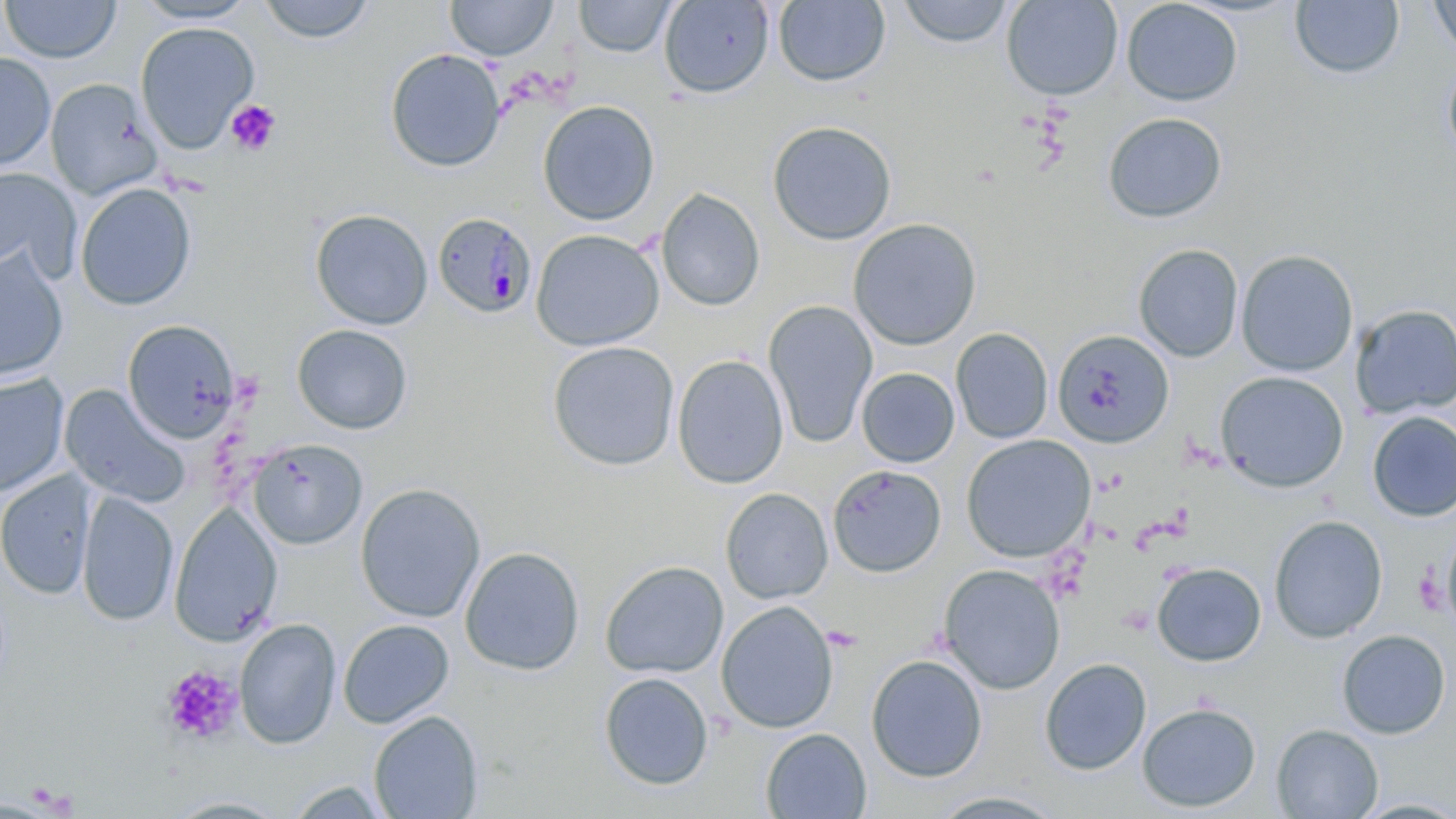 Approximate bounding boxes as named x1/y1/x2/y2 corners in pixels. Platelet locations: (x1=225, y1=100, x2=281, y2=156), (x1=1413, y1=563, x2=1446, y2=620), (x1=161, y1=665, x2=242, y2=744). Uninfected red blood cell locations: (x1=131, y1=0, x2=260, y2=24), (x1=256, y1=0, x2=377, y2=44), (x1=1000, y1=0, x2=1123, y2=101), (x1=1121, y1=0, x2=1243, y2=106), (x1=1427, y1=0, x2=1456, y2=58), (x1=1, y1=1, x2=122, y2=63), (x1=445, y1=1, x2=558, y2=61), (x1=574, y1=1, x2=676, y2=58), (x1=658, y1=1, x2=774, y2=99), (x1=772, y1=1, x2=891, y2=87), (x1=897, y1=1, x2=1014, y2=48), (x1=1290, y1=1, x2=1404, y2=80), (x1=135, y1=21, x2=259, y2=154), (x1=385, y1=48, x2=506, y2=173), (x1=0, y1=51, x2=56, y2=172), (x1=1442, y1=55, x2=1456, y2=164), (x1=45, y1=79, x2=161, y2=199), (x1=537, y1=100, x2=660, y2=226), (x1=1103, y1=112, x2=1227, y2=224), (x1=767, y1=120, x2=897, y2=245), (x1=0, y1=167, x2=82, y2=282), (x1=75, y1=182, x2=197, y2=311), (x1=656, y1=188, x2=765, y2=311), (x1=310, y1=208, x2=433, y2=329), (x1=847, y1=218, x2=982, y2=350), (x1=530, y1=229, x2=665, y2=351), (x1=1134, y1=243, x2=1244, y2=362), (x1=0, y1=249, x2=69, y2=384), (x1=1236, y1=249, x2=1359, y2=377), (x1=763, y1=300, x2=878, y2=448), (x1=1349, y1=305, x2=1456, y2=419), (x1=122, y1=320, x2=242, y2=443), (x1=292, y1=324, x2=413, y2=434), (x1=950, y1=327, x2=1054, y2=444), (x1=1052, y1=329, x2=1174, y2=449), (x1=547, y1=341, x2=680, y2=471), (x1=672, y1=354, x2=789, y2=489), (x1=856, y1=367, x2=959, y2=467), (x1=1215, y1=370, x2=1349, y2=492), (x1=0, y1=373, x2=70, y2=497), (x1=60, y1=385, x2=190, y2=508), (x1=1367, y1=411, x2=1456, y2=522), (x1=961, y1=435, x2=1096, y2=562), (x1=248, y1=438, x2=367, y2=549), (x1=827, y1=465, x2=947, y2=578), (x1=0, y1=470, x2=97, y2=600), (x1=354, y1=483, x2=486, y2=622), (x1=720, y1=488, x2=833, y2=604), (x1=76, y1=491, x2=178, y2=626), (x1=169, y1=502, x2=283, y2=646), (x1=1268, y1=515, x2=1388, y2=643), (x1=1439, y1=532, x2=1456, y2=632), (x1=460, y1=546, x2=584, y2=676), (x1=600, y1=560, x2=729, y2=679), (x1=1152, y1=562, x2=1266, y2=667), (x1=938, y1=563, x2=1066, y2=695), (x1=716, y1=600, x2=838, y2=734), (x1=234, y1=617, x2=342, y2=750), (x1=337, y1=619, x2=455, y2=728), (x1=1336, y1=629, x2=1451, y2=739), (x1=866, y1=654, x2=987, y2=782), (x1=1039, y1=658, x2=1152, y2=775), (x1=599, y1=672, x2=714, y2=791), (x1=1137, y1=702, x2=1261, y2=813), (x1=368, y1=710, x2=483, y2=819), (x1=1271, y1=724, x2=1383, y2=818), (x1=761, y1=728, x2=871, y2=818), (x1=284, y1=779, x2=394, y2=818), (x1=927, y1=791, x2=1068, y2=818). Plasmodium malariae-infected red blood cell locations: (x1=432, y1=212, x2=538, y2=319). Slide-level diagnosis: Plasmodium malariae. May-Grünwald-Giemsa-stained preparation. 1000x magnification. Single field of view. Light microscopy. Thin blood smear. Image is 1456×819 pixels.